Classify this cell by malaria status.
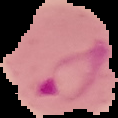
It is parasitized.

image_size: 118×118 pixels
preparation: thin blood smear
image_type: segmented cell region on a black background